State which parasite is depicted.
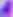
Toxoplasma gondii.

modality = photomicrograph
magnification = 400x